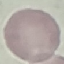

result: no malaria parasites detected
stain: Giemsa
capture: smartphone through the microscope eyepiece
preparation: thin blood smear
image_type: cell patch, automatically extracted from a larger field of view and resized to 64 × 64 pixels